Identify the blood parasite species.
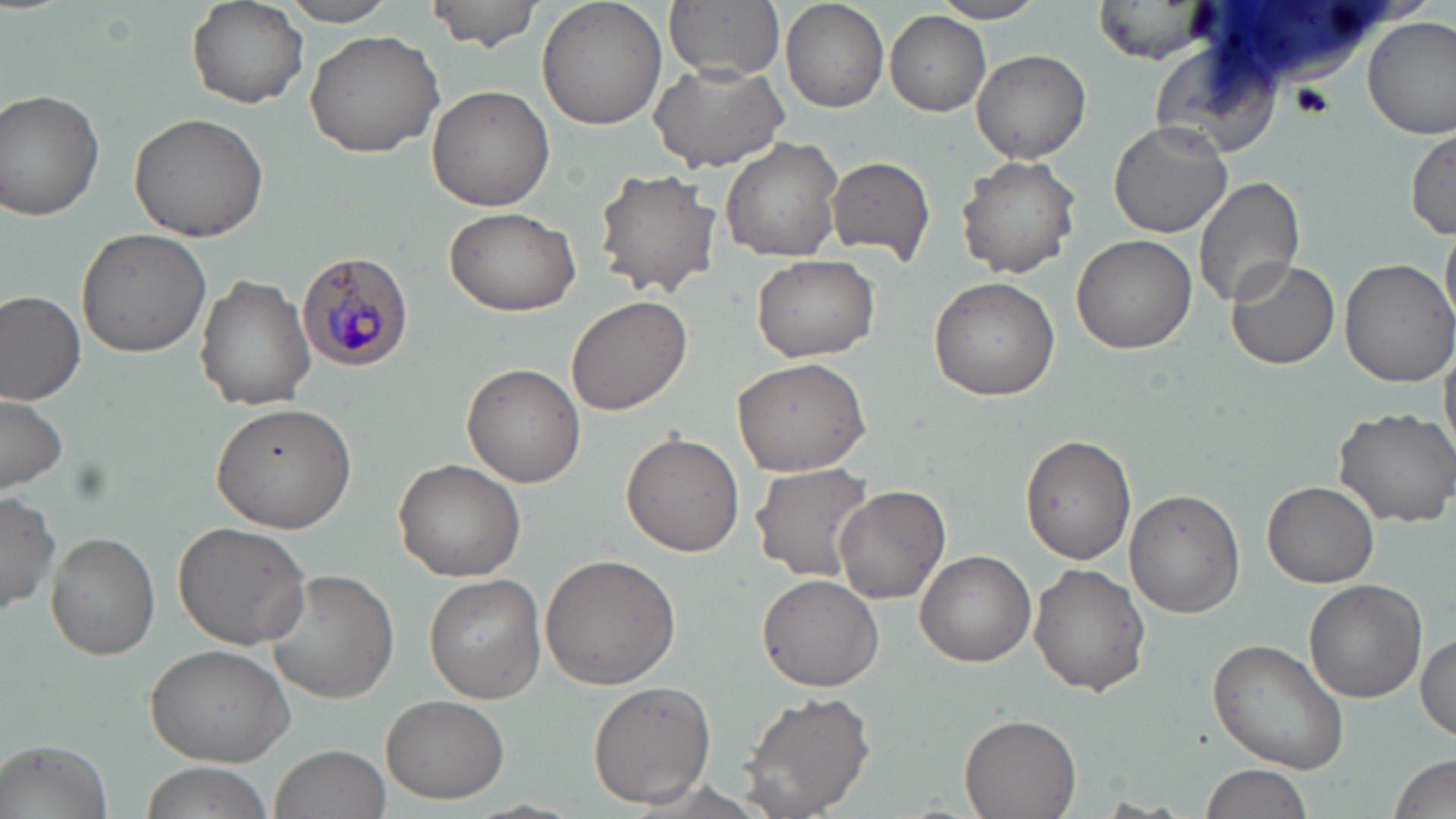
Plasmodium malariae.

{
  "preparation": "thin blood smear",
  "stain": "May-Grünwald-Giemsa",
  "uninfected_red_blood_cell_locations": "approximate bounding boxes as [x1, y1, x2, y2] in pixels: [278, 0, 403, 26], [427, 0, 544, 51], [537, 0, 668, 131], [665, 0, 783, 81], [929, 0, 1046, 24], [1093, 0, 1218, 61], [187, 1, 309, 109], [781, 1, 889, 113], [885, 13, 990, 116], [1364, 16, 1456, 139], [304, 28, 444, 159], [972, 49, 1091, 163], [646, 57, 790, 172], [428, 85, 556, 214], [1, 90, 106, 221], [128, 112, 269, 245], [1108, 120, 1233, 238], [1410, 125, 1456, 239], [721, 138, 846, 262], [956, 154, 1079, 280], [826, 155, 935, 263], [591, 168, 719, 300], [1191, 175, 1305, 311], [443, 207, 581, 316], [1443, 221, 1456, 330], [76, 227, 213, 358], [1072, 234, 1196, 355], [750, 253, 879, 362], [1337, 257, 1455, 389], [1227, 258, 1341, 369], [196, 275, 317, 410], [928, 275, 1059, 400], [0, 291, 86, 404], [565, 294, 691, 417], [1440, 336, 1456, 462], [731, 357, 873, 477], [461, 362, 585, 487], [0, 391, 69, 495], [209, 401, 357, 533], [1333, 407, 1456, 527], [622, 432, 744, 557], [1021, 434, 1136, 564], [395, 458, 527, 581], [750, 462, 877, 582], [1263, 479, 1379, 587], [836, 486, 950, 607], [1122, 489, 1243, 618], [0, 492, 61, 619], [174, 521, 315, 650], [45, 532, 160, 660], [914, 548, 1036, 667], [540, 553, 683, 690], [1029, 563, 1149, 695], [266, 569, 398, 701], [757, 573, 885, 692], [423, 575, 544, 700], [1304, 579, 1427, 703], [1415, 632, 1456, 742], [1208, 637, 1353, 775], [145, 643, 296, 767], [586, 679, 716, 809], [737, 689, 875, 818], [381, 693, 509, 804], [957, 714, 1083, 819], [4, 739, 112, 819], [268, 744, 391, 819], [1388, 754, 1454, 819], [138, 763, 273, 819], [1196, 763, 1313, 819]",
  "image_size": "1456×819 pixels",
  "plasmodium_malariae_infected_red_blood_cell_locations": "approximate bounding boxes as [x1, y1, x2, y2] in pixels: [296, 250, 415, 373]",
  "modality": "light microscopy",
  "field_of_view": "single",
  "magnification": "1000x"
}